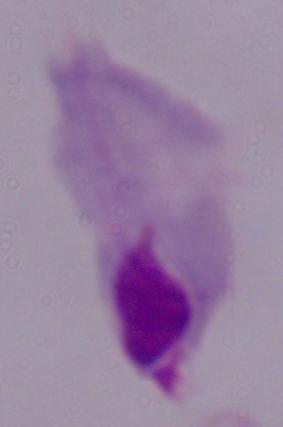

Summary:
  - Modality: micrograph
  - Magnification: 1000x
  - Identification: trichomonad